State which parasite is depicted.
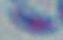

This is Toxoplasma gondii.

magnification = 1000x
modality = photomicrograph